State which parasite is depicted.
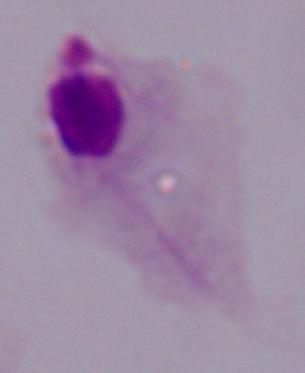

A trichomonad.

Photomicrograph. 1000x magnification.